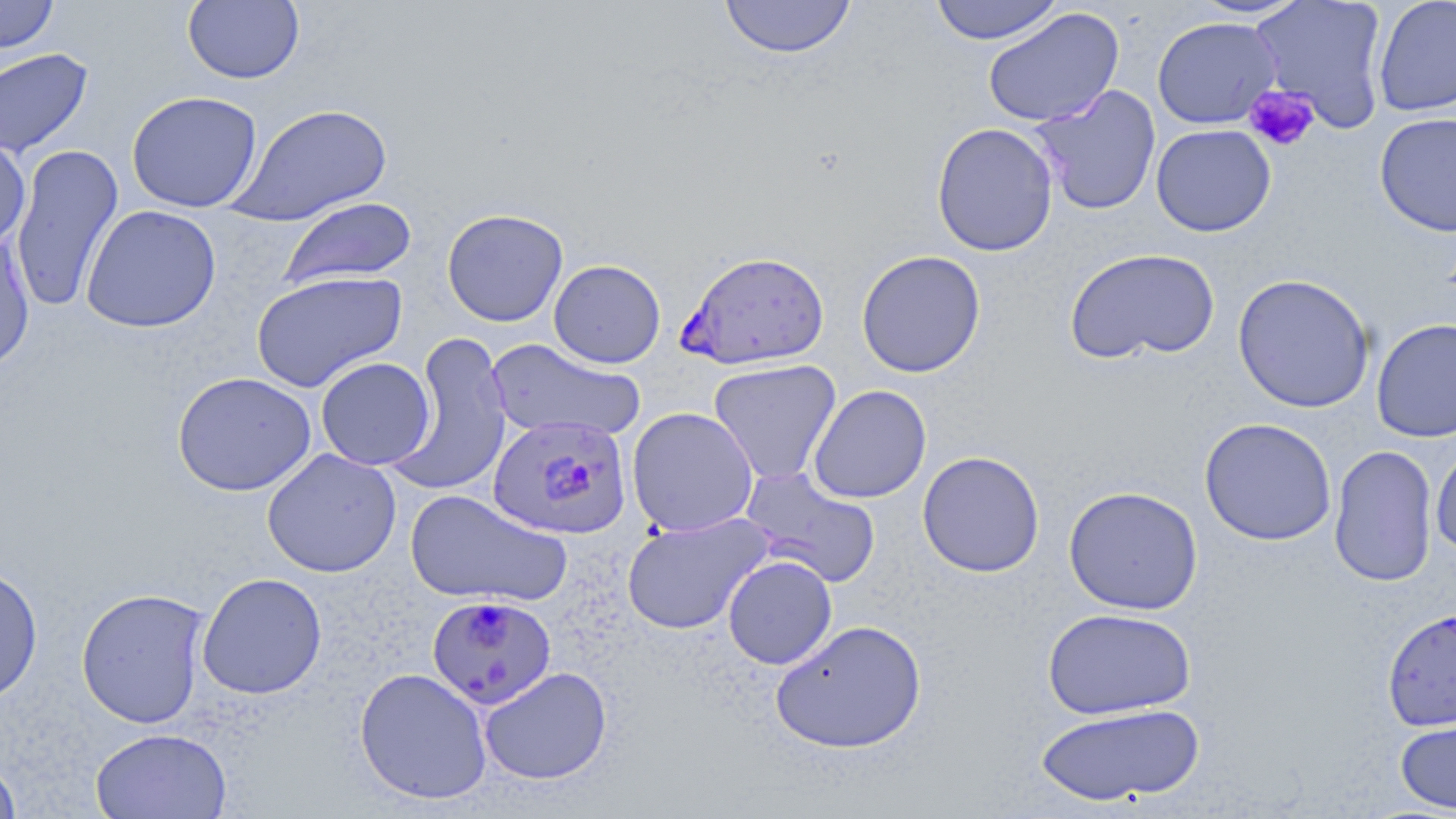

Summary:
  - Coordinate format: approximate bounding boxes as (x1,y1)-(x2,y2) corner pairs in pixels
  - Plasmodium falciparum-infected red blood cell locations: (676,250)-(830,370), (487,413)-(635,539), (426,594)-(556,710)
  - Platelet locations: (1244,85)-(1320,152)
  - Uninfected red blood cell locations: (0,0)-(59,56), (183,0)-(304,84), (719,0)-(856,59), (929,0)-(1064,45), (1188,0)-(1311,19), (1249,0)-(1389,134), (1372,0)-(1456,117), (982,7)-(1125,128), (1152,16)-(1282,129), (0,48)-(94,158), (1030,85)-(1161,217), (126,91)-(263,213), (227,103)-(394,226), (1374,112)-(1456,237), (931,122)-(1059,256), (1151,123)-(1276,237), (0,136)-(31,251), (10,144)-(124,312), (277,196)-(418,290), (81,204)-(221,333), (441,208)-(568,327), (0,228)-(36,375), (1065,247)-(1220,365), (856,250)-(986,378), (549,259)-(666,368), (251,270)-(407,393), (1233,273)-(1375,413), (1371,317)-(1456,443), (390,331)-(513,498), (486,339)-(646,444), (316,357)-(435,470), (708,359)-(842,486), (172,371)-(316,496), (808,385)-(931,503), (626,406)-(759,537), (1199,417)-(1337,546), (1431,442)-(1456,559), (1329,444)-(1438,588), (262,447)-(401,578), (917,450)-(1045,578), (740,468)-(881,588), (1063,485)-(1203,615), (404,488)-(572,607), (622,512)-(774,635), (722,555)-(837,669), (0,564)-(43,703), (196,572)-(327,699), (76,587)-(210,728), (1042,607)-(1197,720), (1382,607)-(1456,731), (770,619)-(927,753), (479,666)-(612,785), (354,667)-(493,805), (1033,702)-(1205,806), (1395,712)-(1456,814), (90,727)-(232,819), (0,756)-(22,819)
  - Slide-level diagnosis: Plasmodium falciparum
  - Field of view: single
  - Preparation: thin blood film
  - Image size: 1456×819 pixels
  - Modality: optical microscopy
  - Stain: May-Grünwald-Giemsa
  - Magnification: 1000x